Locate and identify every blood parasite.
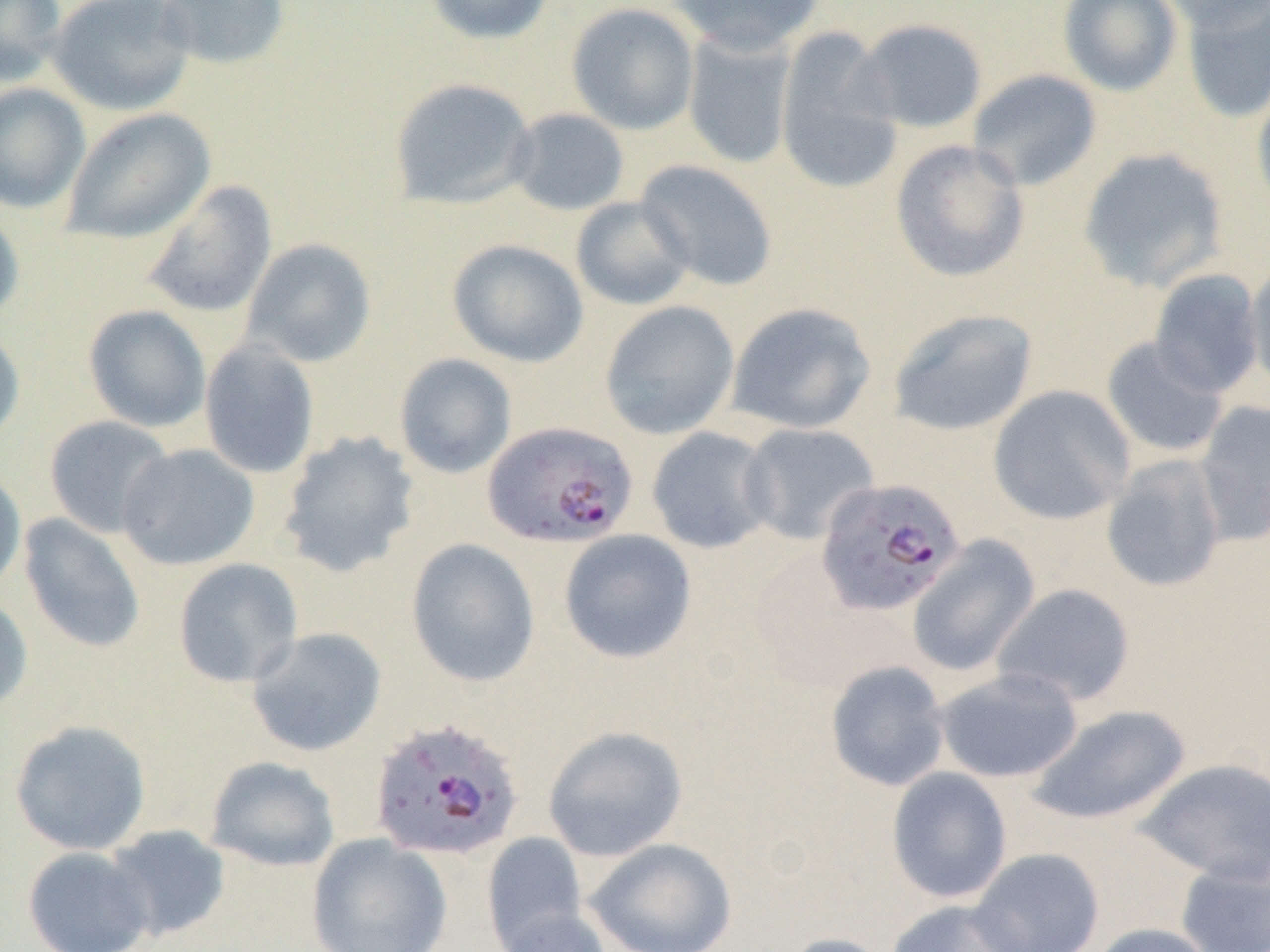
Approximate bounding boxes as [x1, y1, x2, y2] in pixels.
Plasmodium falciparum-infected red blood cells: [482, 420, 639, 548], [816, 477, 966, 617], [368, 717, 526, 863].
No Plasmodium ovale, Plasmodium malariae, Plasmodium vivax, Babesia divergens, or Trypanosoma brucei observed.

slide-level diagnosis = Plasmodium falciparum
image size = 1270×952 pixels
uninfected red blood cell locations = approximate bounding boxes as [x1, y1, x2, y2] in pixels: [0, 0, 66, 86], [47, 0, 195, 116], [154, 0, 291, 71], [423, 0, 556, 45], [665, 0, 826, 55], [1057, 0, 1183, 97], [1156, 0, 1270, 33], [1181, 0, 1269, 123], [566, 2, 699, 135], [853, 18, 988, 134], [773, 26, 905, 195], [682, 30, 797, 169], [968, 69, 1102, 191], [389, 77, 538, 210], [1252, 81, 1270, 217], [0, 83, 90, 213], [61, 107, 215, 245], [506, 107, 630, 216], [889, 139, 1031, 283], [1078, 147, 1229, 292], [634, 159, 779, 291], [141, 180, 278, 318], [570, 195, 696, 311], [0, 208, 25, 325], [242, 238, 377, 367], [447, 238, 589, 367], [1245, 256, 1270, 396], [1149, 269, 1265, 398], [600, 300, 740, 439], [726, 302, 876, 435], [82, 304, 212, 433], [888, 307, 1038, 437], [0, 325, 25, 449], [1100, 336, 1230, 459], [199, 339, 320, 479], [394, 353, 517, 478], [988, 385, 1135, 525], [1194, 399, 1270, 542], [44, 415, 175, 538], [739, 422, 880, 545], [646, 426, 777, 554], [278, 430, 421, 577], [116, 444, 260, 571], [1100, 455, 1227, 593], [0, 466, 27, 596], [17, 513, 147, 654], [558, 529, 697, 664], [906, 536, 1040, 677], [406, 538, 541, 687], [173, 557, 303, 689], [991, 582, 1136, 708], [0, 593, 33, 715], [246, 626, 387, 757], [825, 660, 950, 792], [934, 668, 1083, 783], [1026, 704, 1190, 826], [9, 720, 152, 855], [542, 725, 689, 862], [205, 756, 341, 872], [1136, 758, 1270, 885], [886, 766, 1013, 903], [102, 824, 231, 944], [482, 832, 589, 950], [307, 833, 453, 952], [584, 837, 738, 952], [22, 846, 154, 951], [970, 847, 1104, 952], [1176, 860, 1270, 952], [885, 898, 1035, 952], [493, 906, 614, 952], [1087, 922, 1218, 952], [777, 932, 896, 952]
preparation = thin blood film
field of view = single
magnification = 1000x
modality = optical microscopy